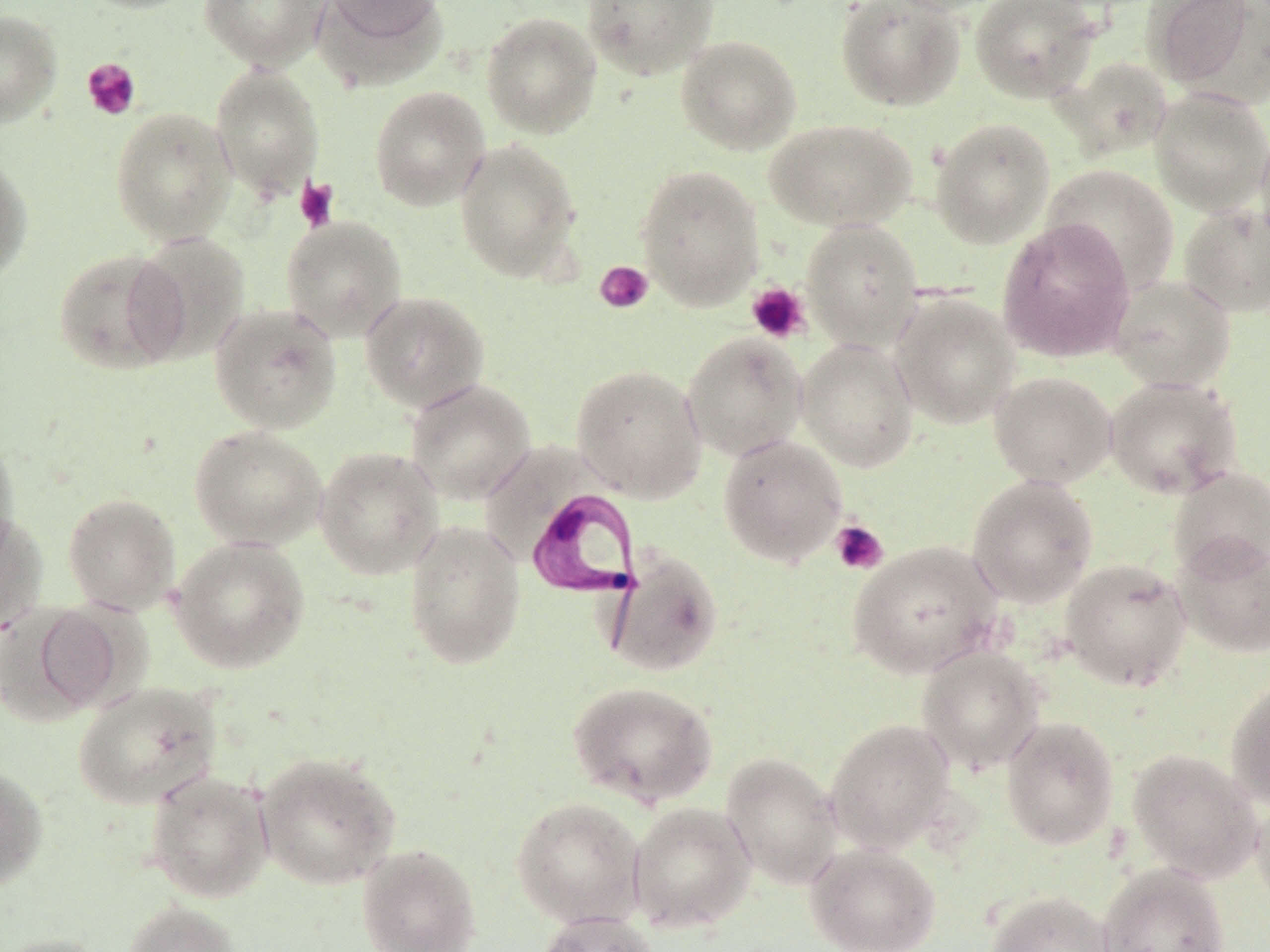

Summary:
  - Coordinate format: approximate bounding boxes as named x1/y1/x2/y2 corners in pixels
  - Platelet locations: (x1=81, y1=58, x2=141, y2=121), (x1=294, y1=176, x2=340, y2=233), (x1=594, y1=260, x2=654, y2=314), (x1=746, y1=282, x2=810, y2=344), (x1=830, y1=519, x2=888, y2=575)
  - Trypanosoma brucei locations: (x1=525, y1=485, x2=647, y2=619)
  - Uninfected red blood cell locations: (x1=77, y1=0, x2=200, y2=14), (x1=199, y1=0, x2=330, y2=70), (x1=314, y1=0, x2=447, y2=87), (x1=325, y1=0, x2=443, y2=44), (x1=581, y1=0, x2=720, y2=80), (x1=834, y1=0, x2=966, y2=111), (x1=885, y1=0, x2=1007, y2=15), (x1=969, y1=0, x2=1101, y2=102), (x1=1143, y1=0, x2=1259, y2=91), (x1=0, y1=9, x2=62, y2=128), (x1=481, y1=11, x2=602, y2=138), (x1=675, y1=35, x2=802, y2=155), (x1=1060, y1=56, x2=1173, y2=159), (x1=210, y1=64, x2=325, y2=199), (x1=369, y1=85, x2=490, y2=211), (x1=1149, y1=89, x2=1270, y2=216), (x1=110, y1=106, x2=237, y2=245), (x1=764, y1=117, x2=917, y2=232), (x1=929, y1=117, x2=1055, y2=249), (x1=1255, y1=128, x2=1270, y2=252), (x1=455, y1=138, x2=582, y2=282), (x1=0, y1=152, x2=33, y2=283), (x1=1042, y1=164, x2=1180, y2=294), (x1=636, y1=166, x2=764, y2=309), (x1=1178, y1=203, x2=1270, y2=318), (x1=280, y1=216, x2=408, y2=342), (x1=998, y1=218, x2=1135, y2=362), (x1=802, y1=219, x2=924, y2=349), (x1=128, y1=232, x2=251, y2=363), (x1=53, y1=249, x2=189, y2=374), (x1=1107, y1=274, x2=1236, y2=393), (x1=359, y1=290, x2=490, y2=412), (x1=890, y1=292, x2=1020, y2=429), (x1=208, y1=303, x2=343, y2=434), (x1=682, y1=331, x2=808, y2=461), (x1=796, y1=337, x2=918, y2=472), (x1=571, y1=364, x2=707, y2=502), (x1=989, y1=371, x2=1117, y2=489), (x1=1104, y1=376, x2=1244, y2=499), (x1=405, y1=378, x2=536, y2=504), (x1=189, y1=425, x2=327, y2=550), (x1=0, y1=432, x2=20, y2=564), (x1=717, y1=434, x2=848, y2=567), (x1=314, y1=446, x2=444, y2=580), (x1=1167, y1=467, x2=1270, y2=581), (x1=967, y1=475, x2=1098, y2=607), (x1=62, y1=493, x2=181, y2=614), (x1=0, y1=511, x2=48, y2=634), (x1=403, y1=521, x2=526, y2=669), (x1=1172, y1=534, x2=1270, y2=658), (x1=169, y1=536, x2=310, y2=674), (x1=848, y1=540, x2=1002, y2=679), (x1=603, y1=549, x2=724, y2=677), (x1=1060, y1=558, x2=1192, y2=692), (x1=9, y1=602, x2=124, y2=719), (x1=916, y1=645, x2=1046, y2=774), (x1=1225, y1=677, x2=1270, y2=809), (x1=73, y1=680, x2=222, y2=810), (x1=568, y1=680, x2=718, y2=807), (x1=1001, y1=716, x2=1120, y2=850), (x1=824, y1=718, x2=956, y2=853), (x1=1127, y1=748, x2=1262, y2=883), (x1=255, y1=752, x2=401, y2=889), (x1=720, y1=752, x2=843, y2=888), (x1=0, y1=764, x2=48, y2=891), (x1=145, y1=769, x2=274, y2=903), (x1=1251, y1=792, x2=1270, y2=910), (x1=511, y1=797, x2=645, y2=927), (x1=628, y1=802, x2=756, y2=933), (x1=804, y1=841, x2=942, y2=952), (x1=356, y1=843, x2=481, y2=952), (x1=1097, y1=864, x2=1229, y2=952), (x1=986, y1=890, x2=1116, y2=952), (x1=123, y1=900, x2=242, y2=952), (x1=533, y1=910, x2=658, y2=952), (x1=0, y1=933, x2=111, y2=952)
  - Slide-level diagnosis: Trypanosoma brucei
  - Preparation: thin blood smear
  - Stain: May-Grünwald-Giemsa
  - Modality: optical microscopy
  - Field of view: one of a larger specimen
  - Image size: 1270×952 pixels
  - Magnification: 1000x